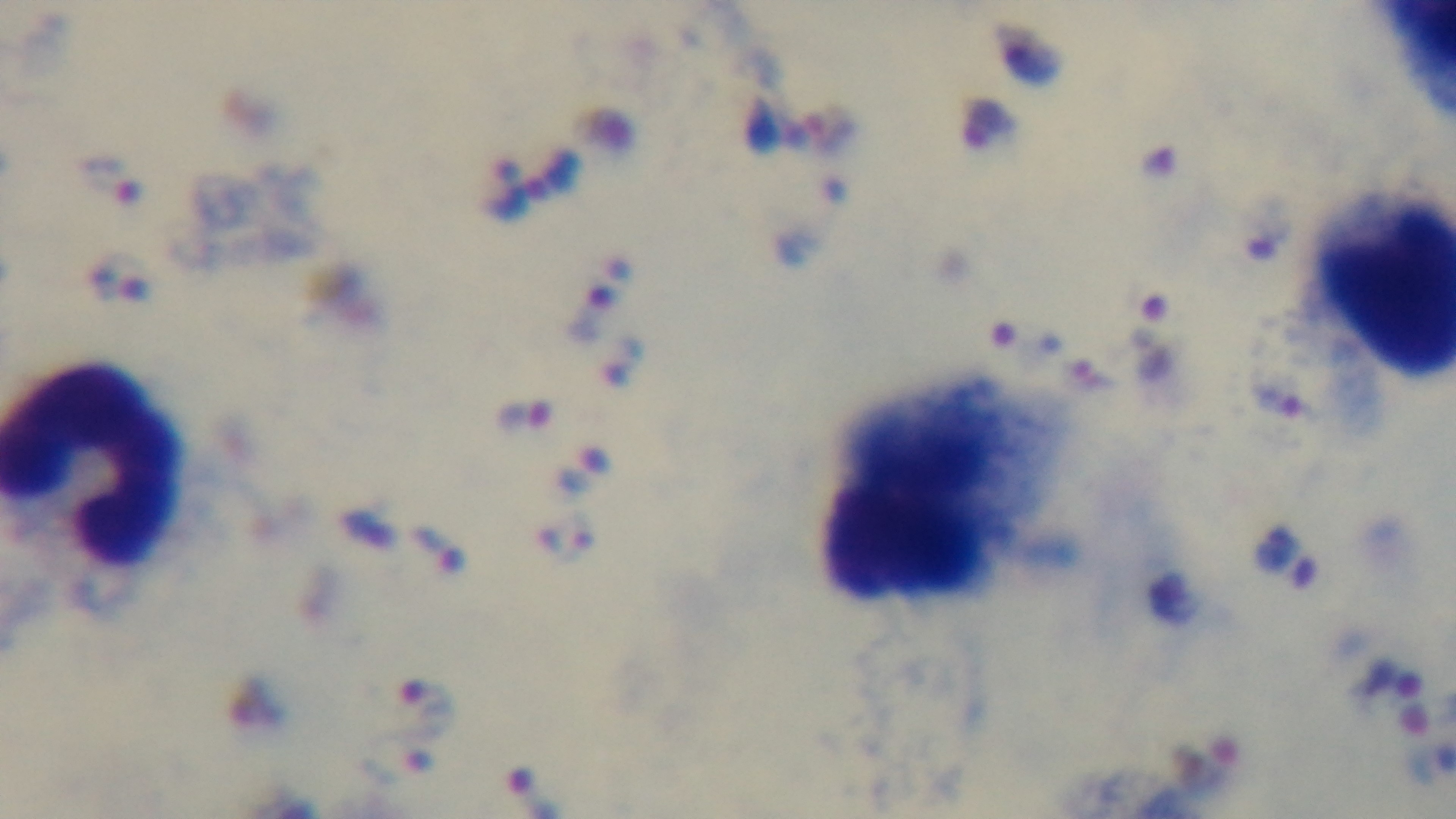

{
  "field_of_view": "one from the slide",
  "malaria_status": "infected",
  "modality": "light microscopy",
  "stain": "Giemsa",
  "objective": "100x oil immersion",
  "capture": "mounted 4K digital camera",
  "preparation": "thick"
}